State which parasite is depicted.
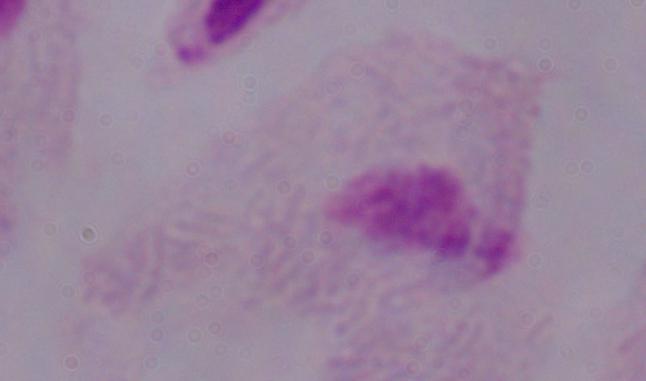
This is a trichomonad.

modality = micrograph
magnification = 1000x